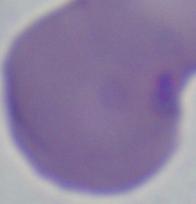
1000x magnification. A Babesia parasite is seen. Photomicrograph.